Locate every uninfected red blood cell.
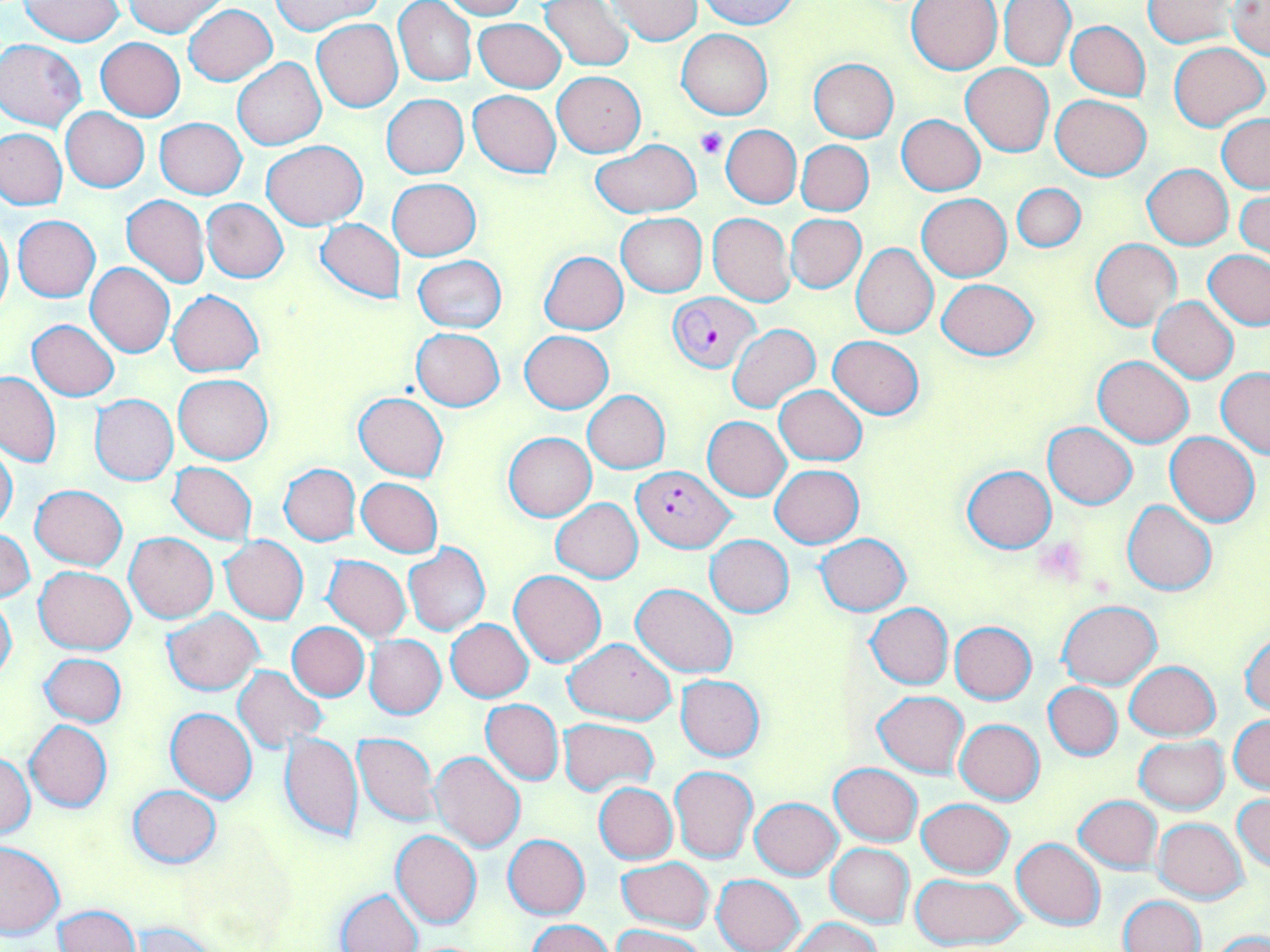

Approximate bounding boxes as (x1, y1, x2, y2) in pixels.
Uninfected red blood cells: (20, 0, 125, 45), (125, 0, 226, 37), (437, 0, 527, 18), (698, 0, 799, 29), (998, 0, 1076, 71), (394, 1, 478, 86), (538, 1, 634, 70), (608, 1, 703, 44), (906, 1, 1002, 74), (1143, 1, 1238, 47), (271, 2, 383, 36), (1228, 2, 1270, 59), (184, 4, 277, 85), (475, 18, 565, 92), (311, 19, 403, 112), (1066, 20, 1150, 101), (677, 29, 772, 119), (96, 37, 185, 121), (1, 39, 86, 129), (1170, 42, 1267, 131), (233, 57, 326, 149), (808, 57, 898, 143), (960, 63, 1054, 157), (553, 72, 645, 156), (468, 89, 561, 178), (1051, 94, 1150, 180), (382, 95, 469, 178), (61, 108, 149, 192), (897, 115, 985, 195), (1217, 115, 1270, 192), (155, 118, 247, 199), (721, 125, 801, 208), (0, 128, 67, 209), (261, 140, 366, 229), (797, 140, 874, 216), (592, 141, 699, 217), (1143, 164, 1233, 249), (388, 179, 481, 260), (1012, 183, 1086, 254), (1235, 191, 1270, 260), (918, 194, 1011, 281), (121, 195, 210, 288), (202, 198, 289, 282), (708, 213, 794, 306), (616, 214, 707, 296), (13, 215, 101, 301), (787, 215, 865, 293), (314, 218, 405, 305), (0, 219, 13, 319), (1091, 239, 1182, 330), (850, 243, 938, 338), (1204, 250, 1270, 330), (540, 251, 628, 334), (413, 256, 507, 334), (86, 263, 175, 357), (936, 277, 1038, 361), (169, 289, 263, 377), (1151, 296, 1238, 383), (28, 319, 118, 401), (727, 322, 820, 413), (411, 328, 505, 410), (521, 331, 613, 413), (829, 336, 924, 418), (1093, 356, 1193, 446), (1216, 369, 1270, 460), (1, 370, 60, 467), (174, 373, 273, 464), (775, 386, 866, 465), (582, 390, 670, 472), (353, 393, 448, 481), (91, 394, 178, 484), (703, 416, 791, 501), (1044, 423, 1137, 508), (504, 432, 596, 521), (1166, 433, 1259, 528), (0, 443, 18, 533), (168, 462, 257, 543), (278, 464, 361, 545), (769, 464, 863, 547), (961, 465, 1057, 553), (357, 478, 444, 557), (30, 484, 127, 569), (550, 498, 643, 583), (1123, 500, 1216, 596), (0, 530, 35, 601), (125, 532, 218, 622), (815, 533, 910, 616), (706, 535, 794, 617), (221, 536, 309, 623), (403, 544, 490, 636), (324, 556, 411, 641), (35, 566, 135, 655), (510, 570, 606, 667), (631, 583, 739, 676), (0, 594, 16, 682), (1057, 601, 1161, 689), (866, 603, 953, 689), (162, 609, 263, 695), (445, 620, 533, 702), (949, 622, 1037, 703), (288, 623, 368, 700), (1240, 631, 1270, 716), (365, 635, 446, 719), (566, 638, 676, 725), (40, 653, 127, 727), (1125, 660, 1222, 740), (234, 666, 327, 753), (676, 674, 764, 760), (1044, 682, 1123, 760), (873, 690, 969, 777), (481, 699, 564, 785), (166, 708, 257, 802), (1229, 715, 1269, 794), (558, 719, 657, 794), (955, 719, 1045, 804), (25, 720, 112, 812), (278, 730, 364, 843), (352, 732, 440, 826), (1135, 737, 1228, 813), (432, 752, 526, 852), (0, 754, 35, 838), (830, 763, 923, 846), (669, 766, 757, 863), (594, 782, 678, 864), (126, 785, 221, 867), (1233, 793, 1269, 873), (1074, 795, 1162, 873), (751, 798, 841, 879), (918, 799, 1013, 878), (1154, 817, 1247, 902), (391, 830, 481, 928), (503, 834, 590, 918), (1012, 838, 1106, 929), (1, 841, 63, 936), (825, 844, 914, 926), (615, 857, 714, 933), (711, 873, 805, 952), (910, 874, 1027, 950), (336, 888, 422, 951), (1119, 895, 1206, 952), (55, 905, 140, 952), (787, 916, 883, 952), (528, 919, 614, 952), (128, 922, 222, 952), (610, 923, 709, 952), (1208, 930, 1270, 951).

Plasmodium falciparum-infected red blood cell locations: (668, 293, 759, 371), (634, 464, 733, 552). Platelet locations: (695, 128, 728, 160). Slide-level diagnosis: Plasmodium falciparum. 1000x magnification. Thin blood smear. Image is 1270×952 pixels. Light microscopy. Single field of view. May-Grünwald-Giemsa-stained preparation.